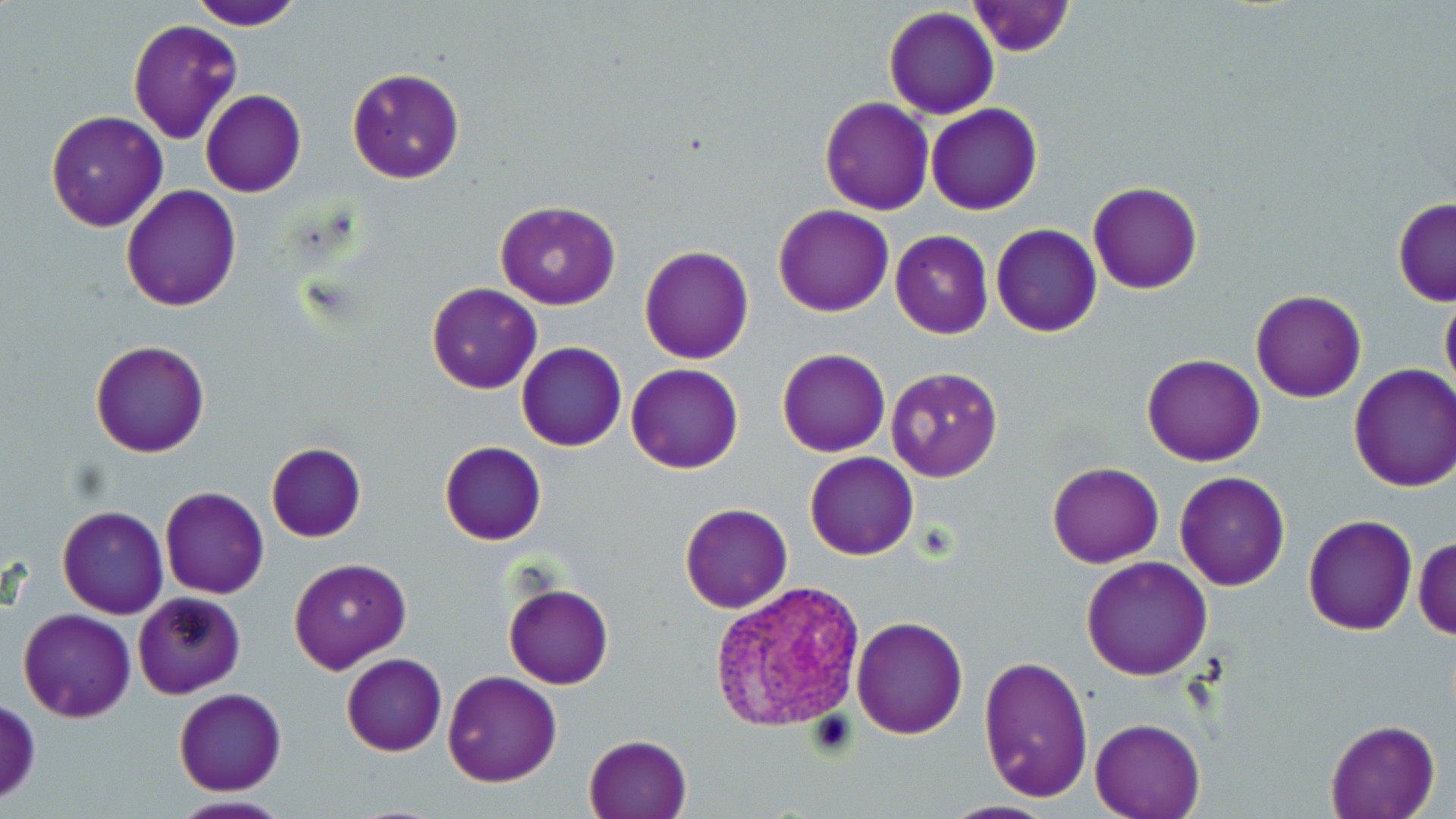 Approximate bounding boxes as [x1, y1, x2, y2] in pixels. Plasmodium vivax-infected red blood cell locations: [711, 579, 868, 731]. Uninfected red blood cell locations: [191, 0, 306, 29], [968, 1, 1073, 56], [884, 6, 999, 119], [127, 19, 242, 144], [171, 49, 300, 173], [346, 66, 466, 185], [200, 90, 306, 197], [819, 96, 934, 214], [928, 103, 1042, 215], [43, 109, 169, 231], [1087, 180, 1204, 295], [121, 184, 242, 312], [1391, 197, 1456, 306], [494, 201, 620, 310], [773, 204, 892, 316], [991, 223, 1102, 338], [891, 230, 993, 339], [639, 245, 754, 364], [427, 282, 543, 395], [1439, 285, 1456, 401], [1250, 289, 1366, 403], [90, 340, 209, 458], [517, 342, 627, 451], [776, 349, 890, 457], [1141, 353, 1266, 465], [626, 362, 743, 474], [1348, 364, 1456, 493], [882, 365, 1003, 484], [439, 441, 546, 546], [265, 442, 366, 543], [804, 452, 919, 560], [1046, 461, 1164, 567], [1174, 471, 1290, 591], [94, 486, 225, 617], [160, 486, 270, 599], [680, 503, 792, 613], [58, 504, 168, 618], [1302, 514, 1418, 636], [1414, 535, 1456, 640], [1081, 555, 1213, 680], [290, 557, 411, 675], [503, 582, 614, 689], [131, 591, 247, 699], [18, 609, 135, 723], [851, 615, 968, 738], [342, 653, 447, 756], [976, 654, 1094, 804], [442, 670, 562, 786], [174, 688, 286, 796], [0, 698, 41, 805], [1089, 717, 1207, 819], [1325, 720, 1438, 819], [583, 732, 691, 818], [167, 796, 296, 819]. Platelet locations: [805, 712, 857, 759]. Slide-level diagnosis: Plasmodium vivax. Optical microscopy. Image is 1456×819 pixels. May-Grünwald-Giemsa stain. Thin blood smear. Single field of view. Captured at 1000x magnification.